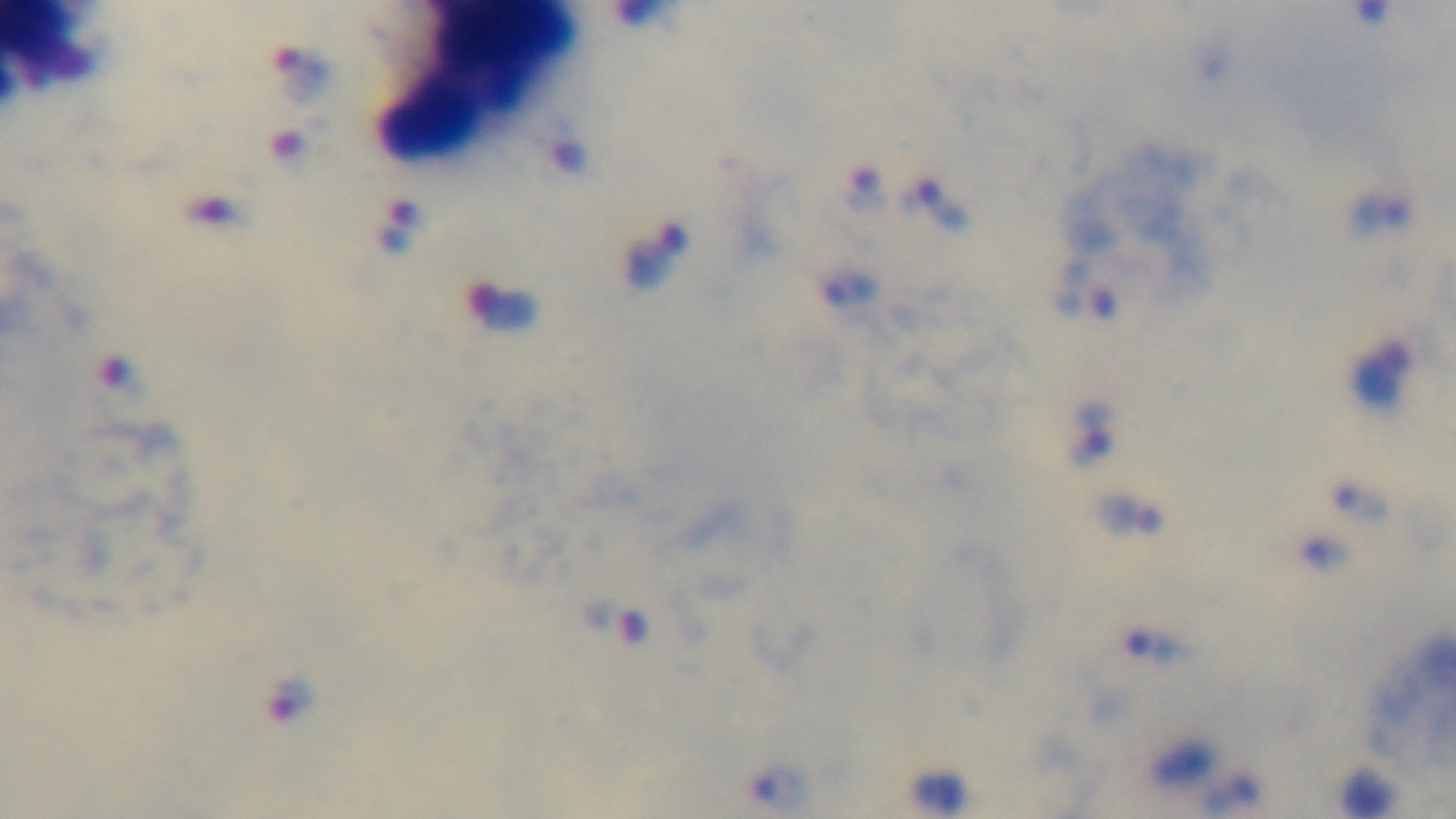
capture = mounted 4K digital camera
malaria status = positive
modality = light microscopy
stain = Giemsa
preparation = thick
objective = 100x oil immersion
field of view = one from the slide